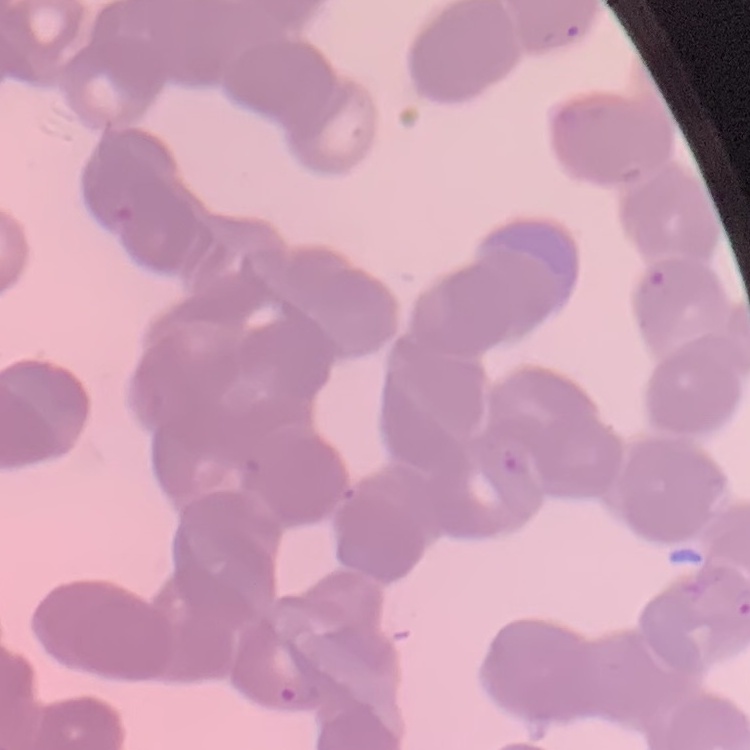

red_blood_cell_morphology: rouleaux formation
image_type: square crop of a larger photomicrograph
preparation: thin peripheral smear
stain: Field's or Giemsa